Assess this cell for malaria.
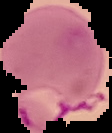

Parasitized.

Summary:
  - Image type: cell region segmented out of the field of view; surrounding area masked to black
  - Image size: 112×133 pixels
  - Preparation: thin blood film